Classify this cell by malaria status.
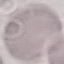

Uninfected.

Acquired by smartphone through the microscope eyepiece. Automatically extracted cell patch, resized to 64 × 64 pixels. Giemsa stain. Thin smear of blood.